Give the extent of all Plasmodium vivax-infected red blood cells.
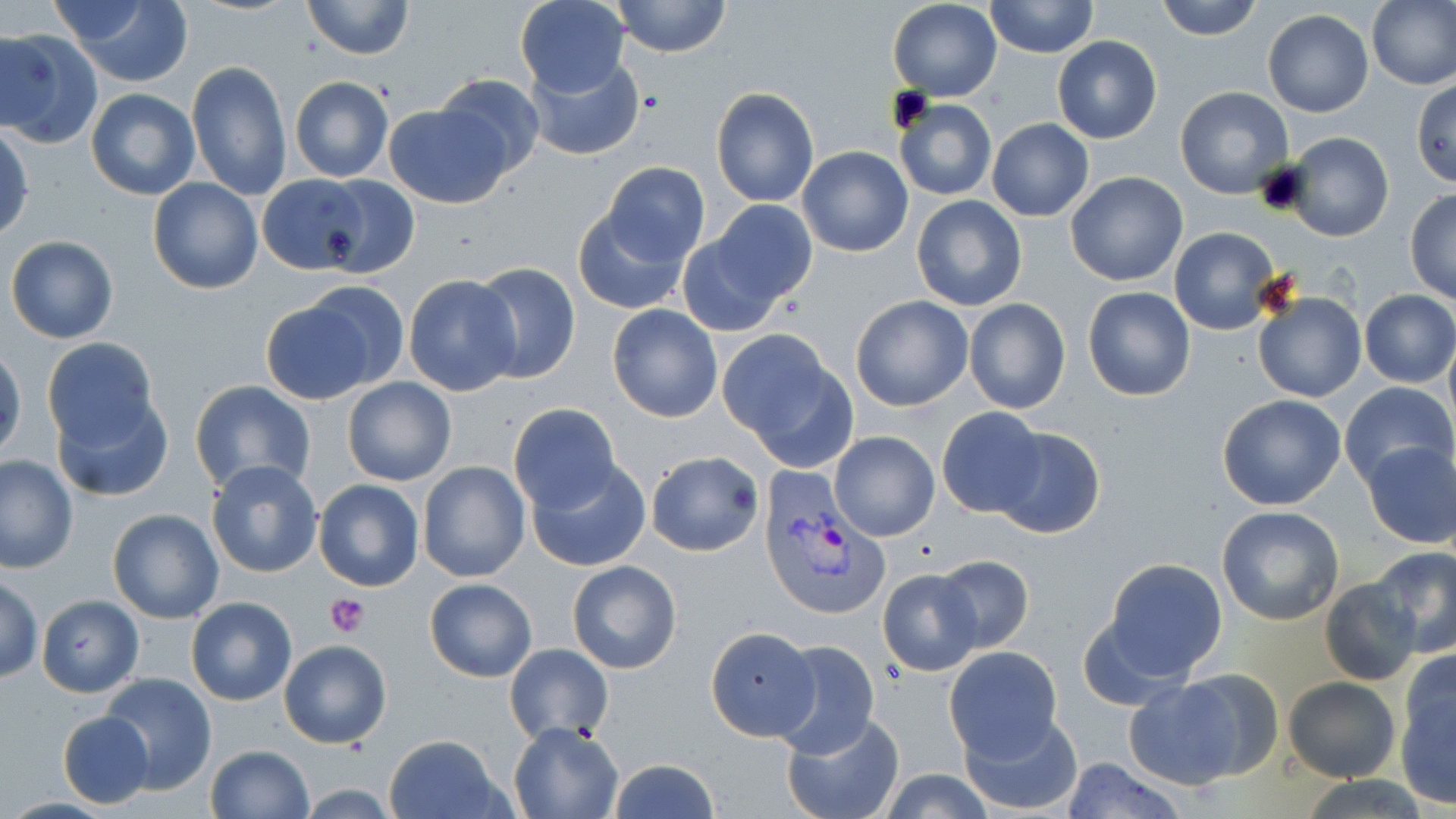
Approximate bounding boxes as named x1/y1/x2/y2 corners in pixels.
Plasmodium vivax-infected red blood cells: (x1=755, y1=466, x2=884, y2=620).

slide-level diagnosis = Plasmodium vivax
modality = light microscopy
platelet locations = approximate bounding boxes as named x1/y1/x2/y2 corners in pixels: (x1=326, y1=593, x2=370, y2=639)
preparation = thin blood film
image size = 1456×819 pixels
uninfected red blood cell locations = approximate bounding boxes as named x1/y1/x2/y2 corners in pixels: (x1=53, y1=0, x2=195, y2=87), (x1=514, y1=0, x2=630, y2=96), (x1=612, y1=0, x2=731, y2=56), (x1=887, y1=0, x2=1001, y2=100), (x1=1154, y1=0, x2=1264, y2=41), (x1=1368, y1=0, x2=1456, y2=91), (x1=301, y1=1, x2=414, y2=59), (x1=984, y1=1, x2=1099, y2=57), (x1=1262, y1=9, x2=1373, y2=117), (x1=0, y1=27, x2=101, y2=147), (x1=1053, y1=35, x2=1161, y2=144), (x1=524, y1=54, x2=644, y2=161), (x1=186, y1=59, x2=294, y2=200), (x1=432, y1=73, x2=546, y2=180), (x1=290, y1=77, x2=394, y2=183), (x1=1411, y1=79, x2=1456, y2=186), (x1=1174, y1=85, x2=1294, y2=199), (x1=710, y1=87, x2=820, y2=207), (x1=85, y1=88, x2=200, y2=201), (x1=893, y1=99, x2=996, y2=201), (x1=383, y1=101, x2=510, y2=209), (x1=987, y1=118, x2=1093, y2=222), (x1=1, y1=122, x2=34, y2=242), (x1=1281, y1=132, x2=1393, y2=241), (x1=796, y1=147, x2=914, y2=257), (x1=602, y1=162, x2=710, y2=266), (x1=1065, y1=171, x2=1189, y2=286), (x1=257, y1=175, x2=372, y2=276), (x1=148, y1=177, x2=262, y2=294), (x1=318, y1=177, x2=420, y2=278), (x1=1405, y1=189, x2=1455, y2=304), (x1=912, y1=194, x2=1027, y2=311), (x1=711, y1=200, x2=818, y2=305), (x1=574, y1=205, x2=691, y2=315), (x1=1168, y1=226, x2=1283, y2=336), (x1=5, y1=236, x2=119, y2=344), (x1=677, y1=236, x2=789, y2=337), (x1=470, y1=263, x2=581, y2=385), (x1=404, y1=274, x2=519, y2=396), (x1=298, y1=280, x2=412, y2=393), (x1=1081, y1=285, x2=1196, y2=401), (x1=1358, y1=289, x2=1456, y2=387), (x1=1250, y1=290, x2=1365, y2=404), (x1=850, y1=295, x2=974, y2=412), (x1=259, y1=298, x2=379, y2=405), (x1=962, y1=298, x2=1070, y2=414), (x1=607, y1=303, x2=723, y2=423), (x1=721, y1=331, x2=847, y2=462), (x1=1443, y1=334, x2=1456, y2=441), (x1=40, y1=337, x2=161, y2=450), (x1=0, y1=344, x2=25, y2=463), (x1=341, y1=376, x2=457, y2=487), (x1=189, y1=380, x2=315, y2=496), (x1=1338, y1=381, x2=1454, y2=491), (x1=54, y1=392, x2=174, y2=501), (x1=1216, y1=393, x2=1348, y2=510), (x1=508, y1=402, x2=622, y2=511), (x1=936, y1=406, x2=1049, y2=519), (x1=988, y1=426, x2=1108, y2=539), (x1=831, y1=430, x2=940, y2=540), (x1=1362, y1=440, x2=1456, y2=549), (x1=645, y1=450, x2=762, y2=556), (x1=0, y1=455, x2=77, y2=573), (x1=526, y1=457, x2=651, y2=572), (x1=205, y1=459, x2=325, y2=580), (x1=416, y1=460, x2=531, y2=582), (x1=313, y1=478, x2=424, y2=592), (x1=1216, y1=506, x2=1345, y2=626), (x1=108, y1=508, x2=225, y2=624), (x1=1370, y1=545, x2=1456, y2=657), (x1=932, y1=555, x2=1034, y2=655), (x1=1101, y1=558, x2=1229, y2=681), (x1=568, y1=560, x2=681, y2=674), (x1=878, y1=569, x2=984, y2=676), (x1=1, y1=576, x2=43, y2=683), (x1=1321, y1=577, x2=1423, y2=685), (x1=425, y1=578, x2=536, y2=682), (x1=37, y1=595, x2=143, y2=697), (x1=186, y1=596, x2=297, y2=706), (x1=706, y1=629, x2=818, y2=743), (x1=279, y1=640, x2=392, y2=749), (x1=770, y1=640, x2=881, y2=757), (x1=504, y1=643, x2=613, y2=744), (x1=944, y1=646, x2=1064, y2=760), (x1=1394, y1=663, x2=1456, y2=807), (x1=1168, y1=668, x2=1286, y2=782), (x1=99, y1=673, x2=217, y2=794), (x1=1282, y1=675, x2=1400, y2=782), (x1=1122, y1=677, x2=1246, y2=789), (x1=959, y1=709, x2=1083, y2=815), (x1=781, y1=710, x2=905, y2=819), (x1=57, y1=711, x2=155, y2=807), (x1=509, y1=723, x2=624, y2=819), (x1=383, y1=732, x2=507, y2=818), (x1=205, y1=744, x2=315, y2=819), (x1=1059, y1=756, x2=1185, y2=819), (x1=606, y1=758, x2=720, y2=819), (x1=878, y1=772, x2=996, y2=818)
magnification = 1000x
stain = May-Grünwald-Giemsa
field of view = single